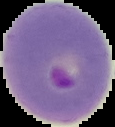

{
  "image_type": "segmented cell region on a black background",
  "preparation": "thin blood smear",
  "image_size": "115×127 pixels",
  "result": "Plasmodium parasites detected"
}